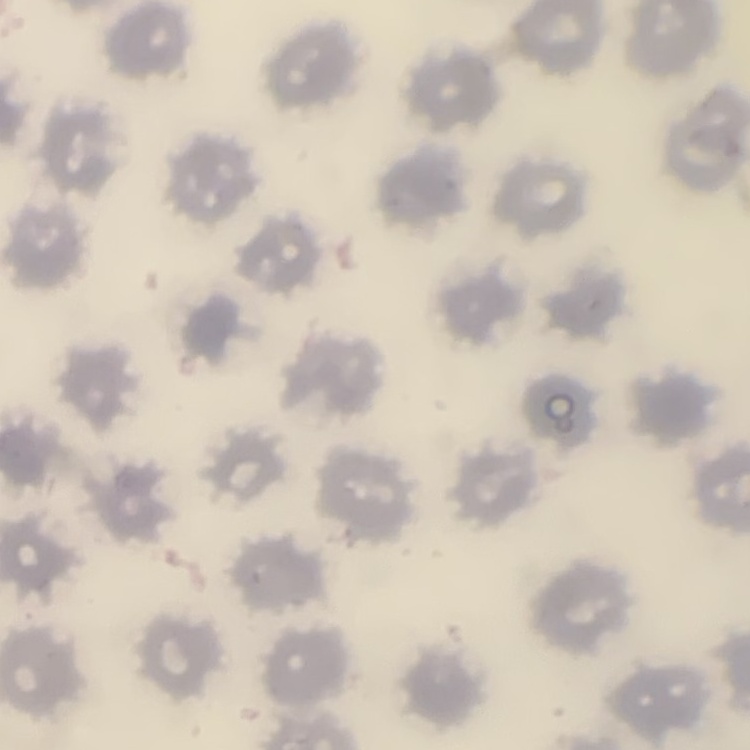 The red blood cells show no rouleaux formation. Thin blood smear. Field's or Giemsa stain. Square crop of a larger photomicrograph.